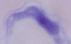
magnification = 1000x
identification = trypanosome
modality = photomicrograph